Report the malaria status of this cell.
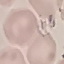

It is uninfected.

{
  "preparation": "thin blood smear",
  "capture": "smartphone camera at the microscope eyepiece",
  "image_type": "automatically extracted cell patch, resized to 64 × 64 pixels",
  "stain": "Giemsa"
}